Name the parasite shown.
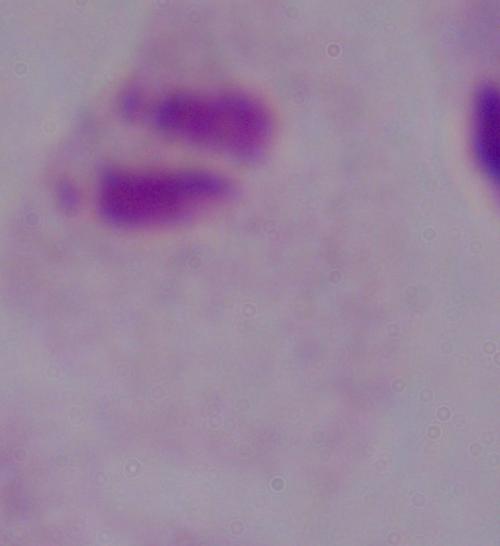

This is a trichomonad.

Summary:
  - Modality: micrograph
  - Magnification: 1000x